Outline each uninfected red blood cell.
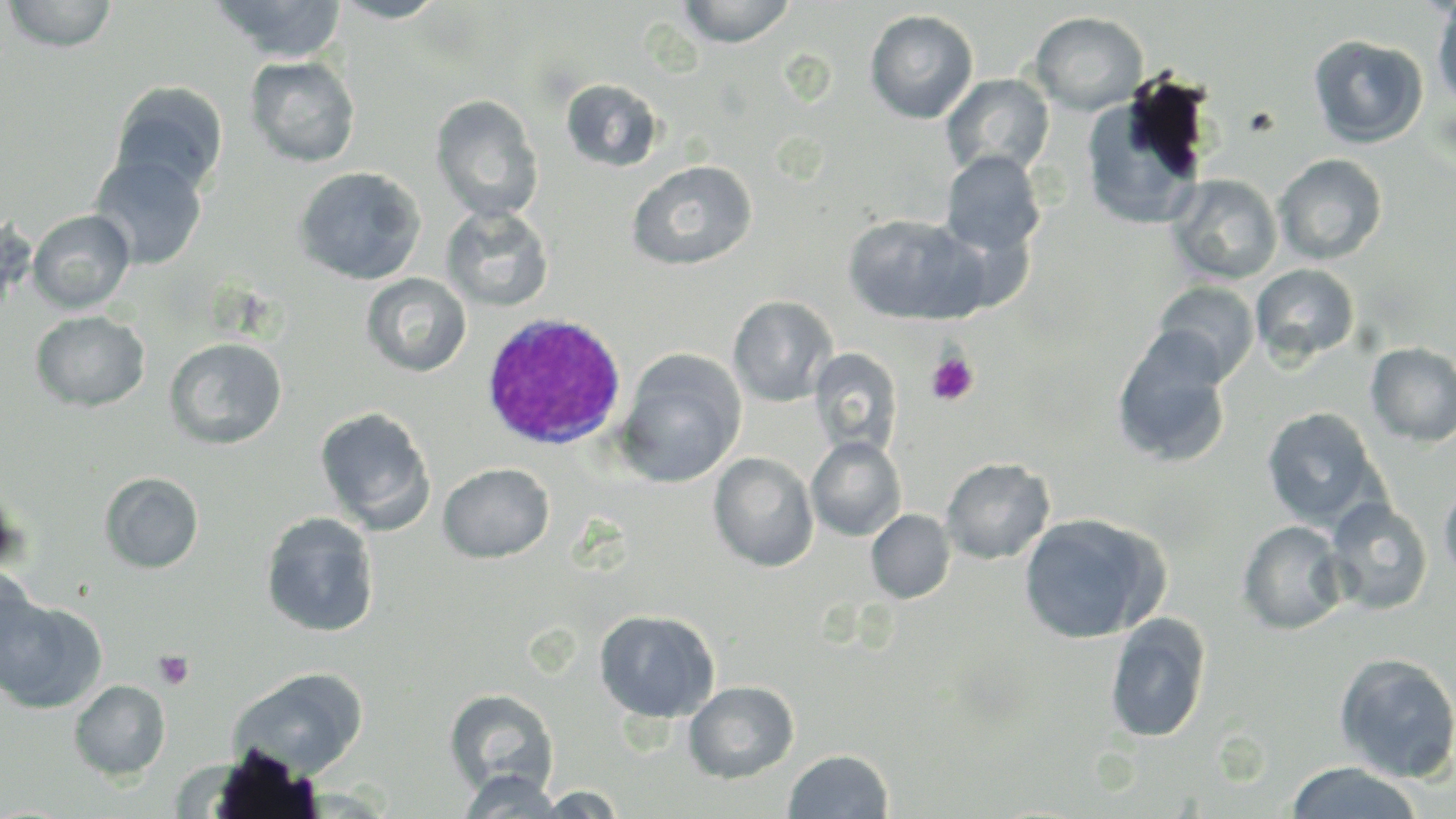

Approximate bounding boxes as named x1/y1/x2/y2 corners in pixels.
Uninfected red blood cells: (x1=2, y1=0, x2=119, y2=52), (x1=209, y1=0, x2=348, y2=62), (x1=331, y1=0, x2=450, y2=23), (x1=678, y1=0, x2=796, y2=47), (x1=1431, y1=3, x2=1456, y2=115), (x1=865, y1=10, x2=979, y2=123), (x1=1030, y1=11, x2=1148, y2=115), (x1=1307, y1=34, x2=1429, y2=148), (x1=245, y1=56, x2=360, y2=168), (x1=941, y1=73, x2=1054, y2=179), (x1=560, y1=78, x2=664, y2=173), (x1=109, y1=81, x2=229, y2=197), (x1=1080, y1=88, x2=1210, y2=229), (x1=430, y1=94, x2=543, y2=223), (x1=941, y1=150, x2=1045, y2=259), (x1=1274, y1=153, x2=1387, y2=265), (x1=89, y1=154, x2=208, y2=270), (x1=626, y1=160, x2=758, y2=270), (x1=294, y1=167, x2=426, y2=285), (x1=1167, y1=174, x2=1283, y2=285), (x1=440, y1=205, x2=555, y2=311), (x1=27, y1=209, x2=135, y2=313), (x1=842, y1=212, x2=985, y2=325), (x1=1252, y1=263, x2=1360, y2=364), (x1=361, y1=273, x2=472, y2=377), (x1=1151, y1=280, x2=1260, y2=385), (x1=728, y1=295, x2=838, y2=406), (x1=30, y1=310, x2=150, y2=412), (x1=1112, y1=330, x2=1232, y2=469), (x1=163, y1=337, x2=288, y2=450), (x1=1365, y1=342, x2=1456, y2=447), (x1=809, y1=347, x2=902, y2=457), (x1=616, y1=350, x2=746, y2=488), (x1=314, y1=407, x2=436, y2=533), (x1=1261, y1=407, x2=1382, y2=528), (x1=806, y1=436, x2=906, y2=541), (x1=708, y1=452, x2=819, y2=571), (x1=941, y1=457, x2=1055, y2=564), (x1=438, y1=462, x2=554, y2=563), (x1=99, y1=471, x2=204, y2=573), (x1=1438, y1=480, x2=1456, y2=589), (x1=0, y1=483, x2=28, y2=577), (x1=1325, y1=497, x2=1433, y2=616), (x1=866, y1=509, x2=956, y2=604), (x1=260, y1=512, x2=380, y2=637), (x1=1018, y1=513, x2=1166, y2=644), (x1=1237, y1=520, x2=1349, y2=635), (x1=0, y1=566, x2=39, y2=682), (x1=0, y1=595, x2=106, y2=714), (x1=594, y1=609, x2=720, y2=723), (x1=1104, y1=612, x2=1212, y2=744), (x1=1334, y1=652, x2=1456, y2=783), (x1=229, y1=667, x2=369, y2=777), (x1=69, y1=679, x2=170, y2=780), (x1=683, y1=680, x2=799, y2=783), (x1=444, y1=688, x2=559, y2=798), (x1=784, y1=749, x2=893, y2=818), (x1=1284, y1=761, x2=1425, y2=818), (x1=458, y1=770, x2=565, y2=818), (x1=531, y1=786, x2=629, y2=817).

Summary:
  - White blood cell locations: (x1=479, y1=312, x2=627, y2=451)
  - Platelet locations: (x1=925, y1=352, x2=979, y2=406), (x1=153, y1=650, x2=194, y2=690)
  - Slide-level diagnosis: Plasmodium ovale
  - Modality: optical microscopy
  - Stain: May-Grünwald-Giemsa
  - Magnification: 1000x
  - Field of view: single
  - Image size: 1456×819 pixels
  - Preparation: thin blood smear